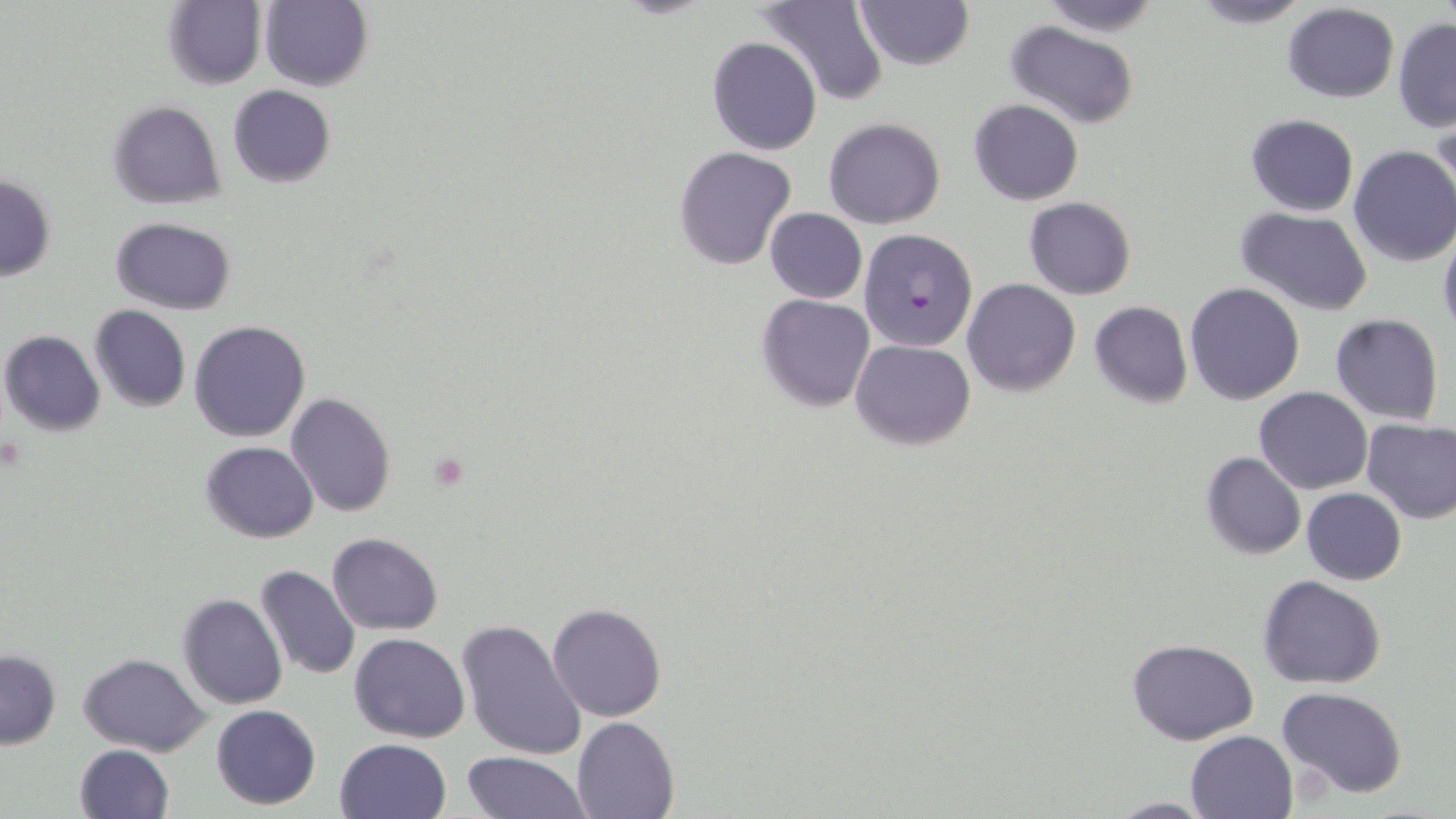 Approximate bounding boxes as (x1, y1, x2, y2) in pixels. Uninfected red blood cell locations: (259, 0, 373, 91), (1040, 0, 1165, 36), (1186, 0, 1314, 29), (162, 1, 265, 89), (757, 1, 890, 105), (854, 1, 975, 72), (1282, 3, 1399, 103), (1393, 18, 1456, 132), (1005, 22, 1141, 129), (707, 36, 821, 156), (228, 84, 336, 187), (968, 99, 1083, 204), (106, 100, 227, 208), (1245, 113, 1359, 217), (1430, 113, 1454, 213), (823, 118, 945, 229), (1348, 145, 1456, 267), (674, 146, 796, 268), (0, 174, 56, 281), (1024, 196, 1136, 299), (1234, 206, 1375, 314), (764, 208, 867, 302), (110, 217, 235, 314), (1437, 228, 1456, 338), (961, 278, 1081, 395), (1184, 281, 1305, 404), (756, 294, 874, 412), (1089, 301, 1193, 408), (90, 306, 191, 413), (1330, 314, 1444, 424), (189, 319, 310, 442), (1, 330, 105, 436), (851, 338, 974, 450), (1254, 387, 1373, 493), (285, 391, 396, 518), (1360, 416, 1456, 523), (199, 441, 319, 544), (1200, 451, 1305, 559), (1300, 487, 1405, 585), (327, 532, 444, 635), (254, 565, 360, 680), (1258, 575, 1387, 690), (178, 592, 286, 709), (548, 602, 666, 721), (456, 616, 586, 760), (350, 634, 469, 742), (1126, 638, 1259, 746), (0, 649, 61, 749), (79, 652, 209, 755), (1277, 686, 1408, 798), (211, 704, 321, 809), (572, 715, 680, 818), (1186, 730, 1297, 819), (335, 738, 452, 819), (73, 744, 174, 819), (462, 751, 587, 819), (1102, 796, 1218, 817). Platelet locations: (426, 451, 472, 491). Plasmodium falciparum-infected red blood cell locations: (858, 228, 978, 352). Slide-level diagnosis: Plasmodium falciparum. Image is 1456×819 pixels. Optical microscopy. May-Grünwald-Giemsa stain. Thin blood film. Single field of view. 1000x magnification.